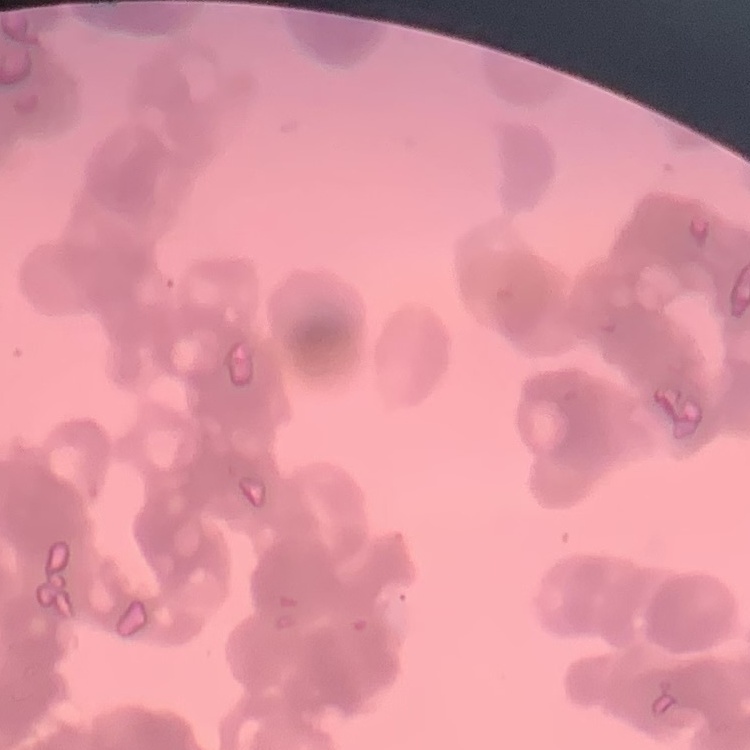
{
  "red_blood_cell_morphology": "rouleaux formation",
  "preparation": "thin peripheral smear",
  "image_type": "one tile cut from a larger photomicrograph",
  "stain": "Field's or Giemsa"
}